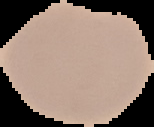
From a thin blood film. Result: malaria parasites detected. Cell region segmented out of the field of view; the surrounding area is masked to black. Image is 154×127 pixels.